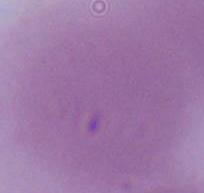
modality = micrograph
magnification = 1000x
identification = red blood cell